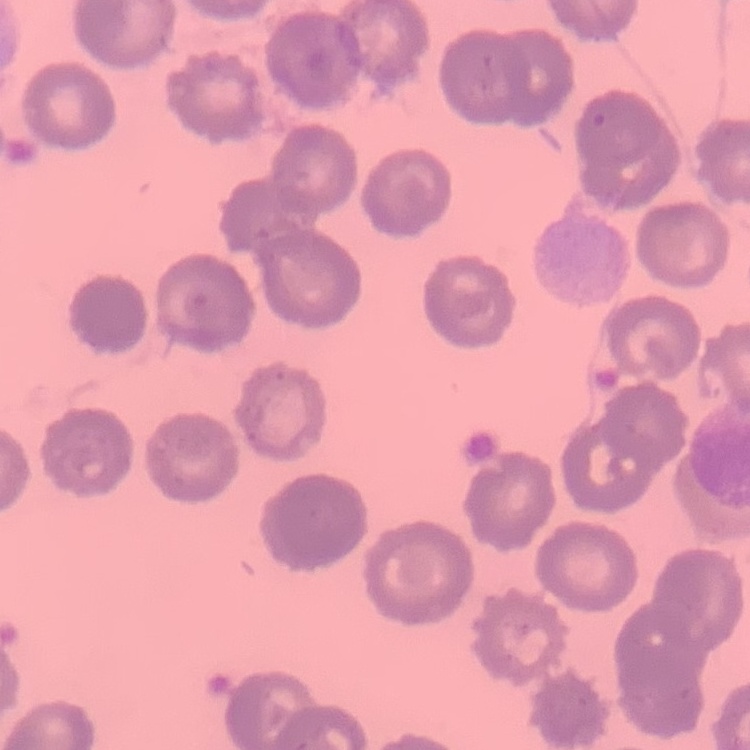

erythrocyte morphology = no rouleaux formation
image type = square crop of a larger photomicrograph
preparation = thin peripheral smear
stain = Field's or Giemsa